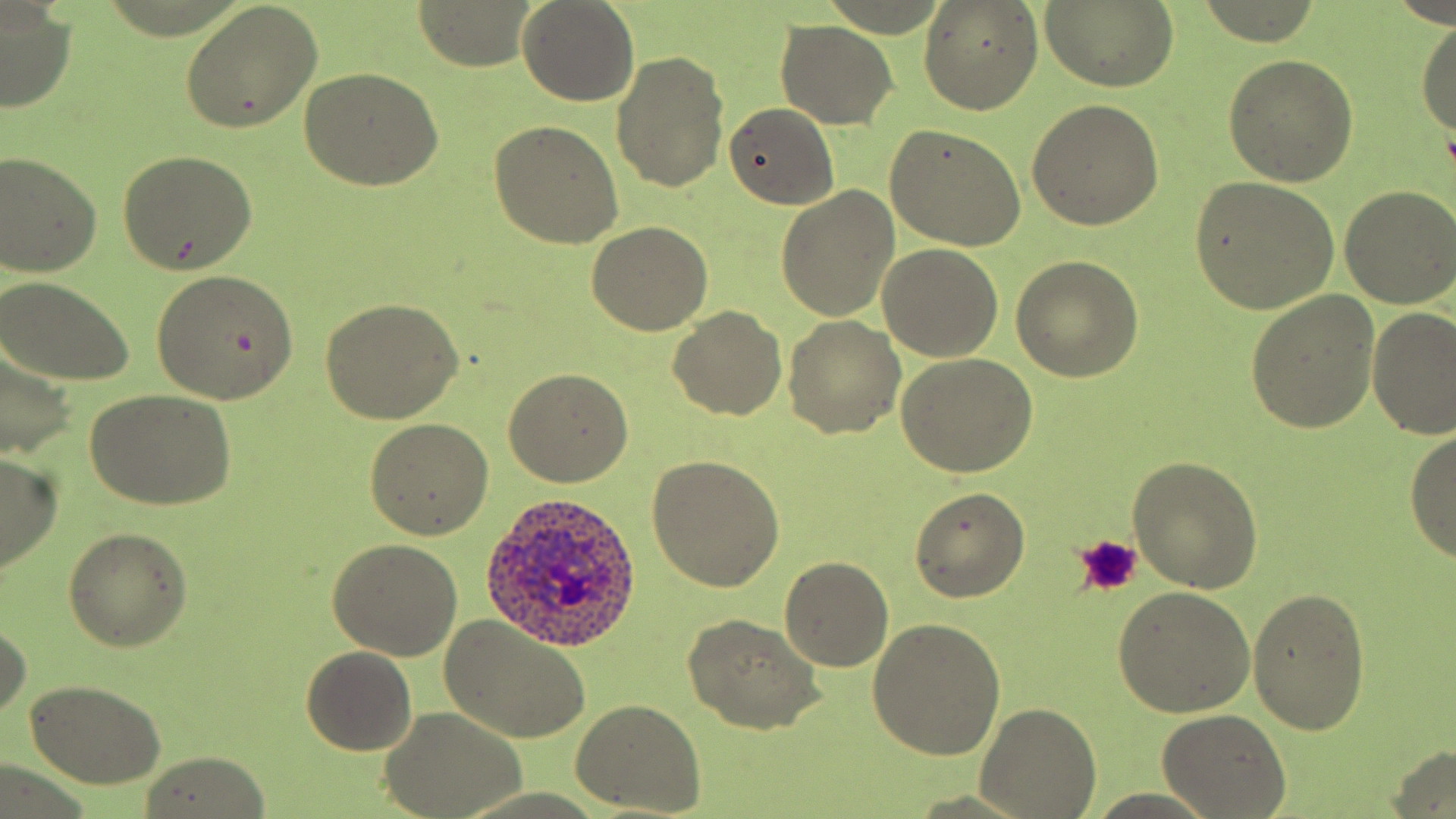

slide_level_diagnosis: Plasmodium ovale
uninfected_red_blood_cell_locations: 'approximate bounding boxes as (x1,y1)-(x2,y2) corner pairs in pixels: (518,0)-(638,106), (918,1)-(1043,115), (181,2)-(324,132), (415,2)-(536,70), (1041,2)-(1178,91), (0,8)-(75,114), (1415,15)-(1456,147), (776,21)-(896,130), (612,51)-(729,194), (1223,55)-(1358,186), (299,68)-(445,190), (1028,98)-(1165,230), (725,103)-(840,209), (488,122)-(623,249), (884,124)-(1027,251), (118,152)-(258,277), (0,153)-(102,277), (1188,175)-(1340,317), (779,186)-(899,321), (1338,186)-(1455,308), (586,219)-(714,335), (876,244)-(1004,363), (1011,255)-(1143,382), (151,270)-(299,402), (0,275)-(136,389), (1247,290)-(1381,432), (319,298)-(463,424), (670,305)-(786,421), (1366,305)-(1455,442), (784,317)-(905,440), (0,336)-(80,461), (899,355)-(1037,477), (503,366)-(633,487), (84,389)-(236,511), (365,416)-(494,538), (1405,426)-(1456,564), (0,451)-(62,570), (1127,454)-(1263,596), (648,457)-(784,592), (909,487)-(1030,603), (63,528)-(191,651), (327,540)-(462,662), (781,556)-(893,671), (1114,587)-(1254,716), (1247,588)-(1371,734), (0,613)-(29,724), (440,615)-(590,743), (684,616)-(824,735), (866,617)-(1007,760), (301,646)-(417,755), (26,678)-(168,787), (572,699)-(708,816), (977,703)-(1100,819), (382,708)-(527,819), (1160,709)-(1291,817), (1387,744)-(1456,819), (140,754)-(271,817)'
modality: optical microscopy
plasmodium_ovale_infected_red_blood_cell_locations: 'approximate bounding boxes as (x1,y1)-(x2,y2) corner pairs in pixels: (479,495)-(647,659)'
platelet_locations: 'approximate bounding boxes as (x1,y1)-(x2,y2) corner pairs in pixels: (1075,531)-(1143,597)'
magnification: 1000x
preparation: thin blood smear
stain: May-Grünwald-Giemsa
field_of_view: single
image_size: 1456×819 pixels